State which parasite is depicted.
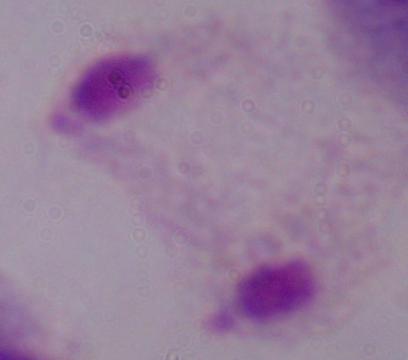
A trichomonad.

{
  "magnification": "1000x",
  "modality": "photomicrograph"
}